Assess this cell for malaria.
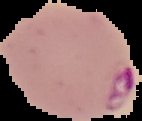

Parasitized.

Segmented cell region on a black background. Image is 142×121 pixels. From a thin blood film.